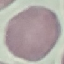
Summary:
  - Malaria status: uninfected
  - Preparation: thin blood smear
  - Capture: smartphone camera at the microscope eyepiece
  - Image type: automatically extracted cell patch, resized to 64 × 64 pixels
  - Stain: Giemsa